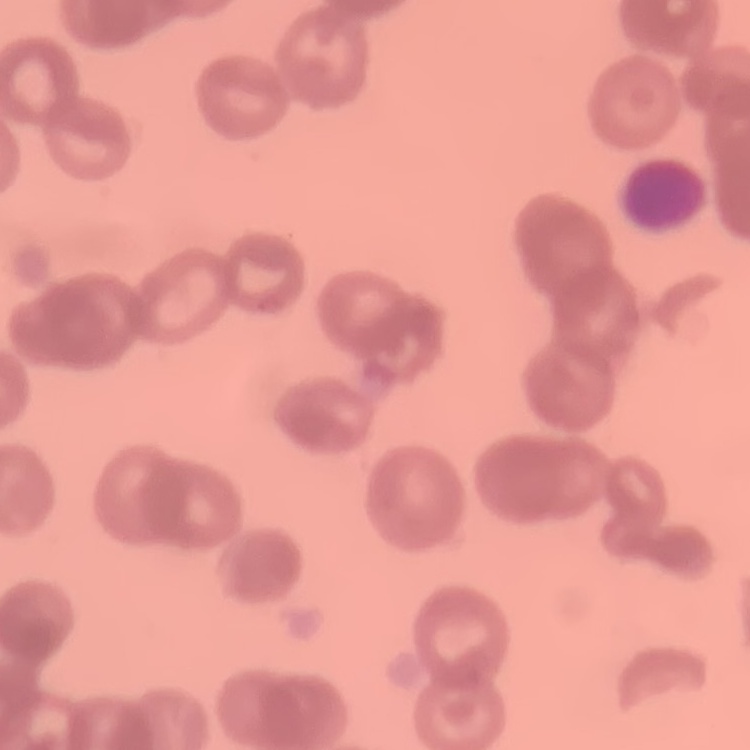

Summary:
  - Red blood cell morphology: rouleaux formation
  - Image type: one tile cut from a larger photomicrograph
  - Preparation: thin blood film
  - Stain: Field's or Giemsa